Comment on the background quality.
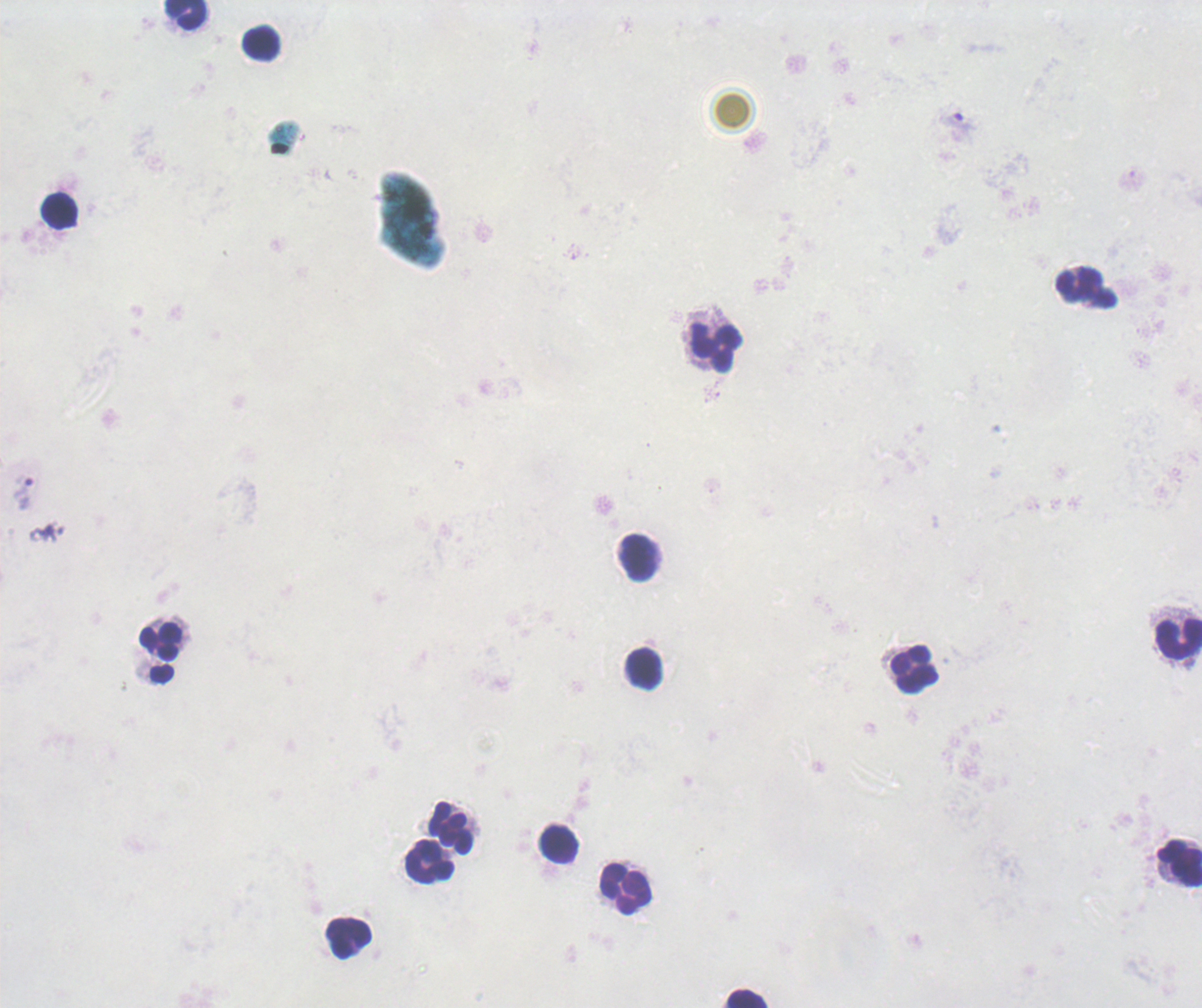

Unsatisfactory.

coordinate format = approximate centers as (x, y) in pixels
leukocyte locations = (184, 14), (262, 42), (59, 211), (1085, 288), (715, 348), (638, 557), (1179, 638), (160, 643), (643, 669), (915, 669), (451, 827), (559, 845), (428, 861), (1179, 863), (625, 888), (348, 938), (746, 997)
trophozoite locations = (957, 125), (23, 493)
result = positive for Plasmodium parasites
preparation = thick smear of blood
image size = 1202×1008 pixels
context = previously used in an actual diagnosis
magnification = 100x
stain = Romanowsky
field of view = single